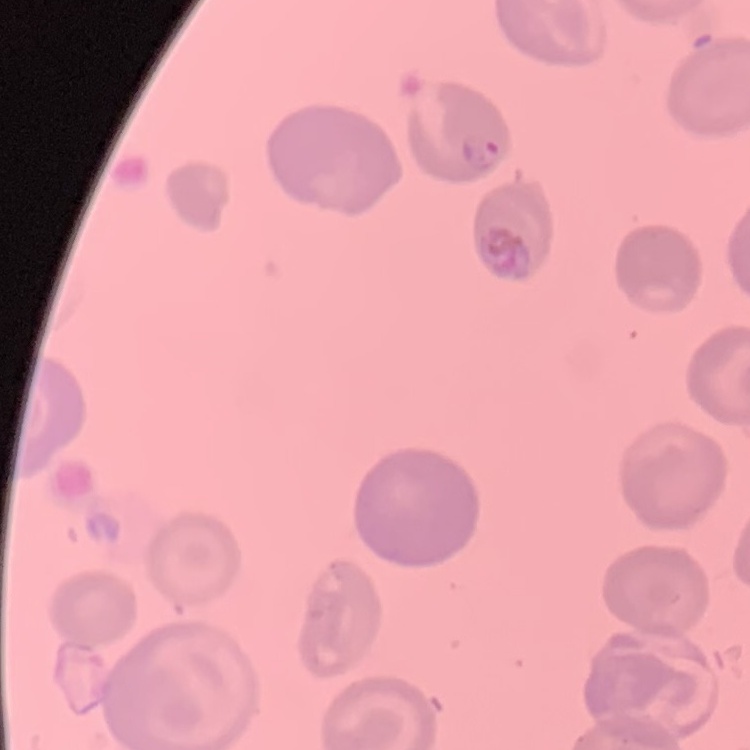

red_blood_cell_morphology: no rouleaux formation
image_type: square crop of a larger photomicrograph
stain: Field's or Giemsa
preparation: thin blood smear